Identify the parasite.
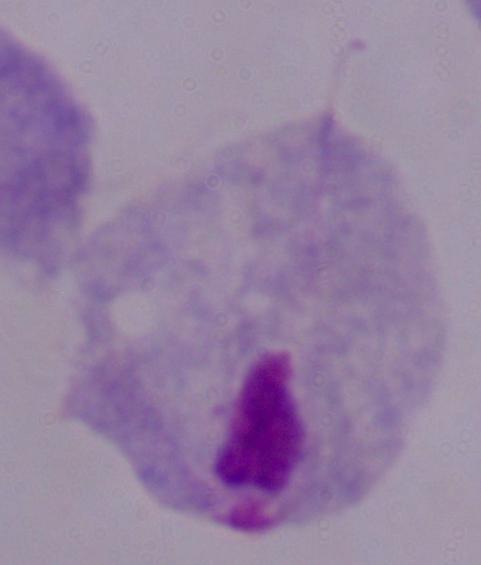

This is a trichomonad.

Summary:
  - Modality: photomicrograph
  - Magnification: 1000x